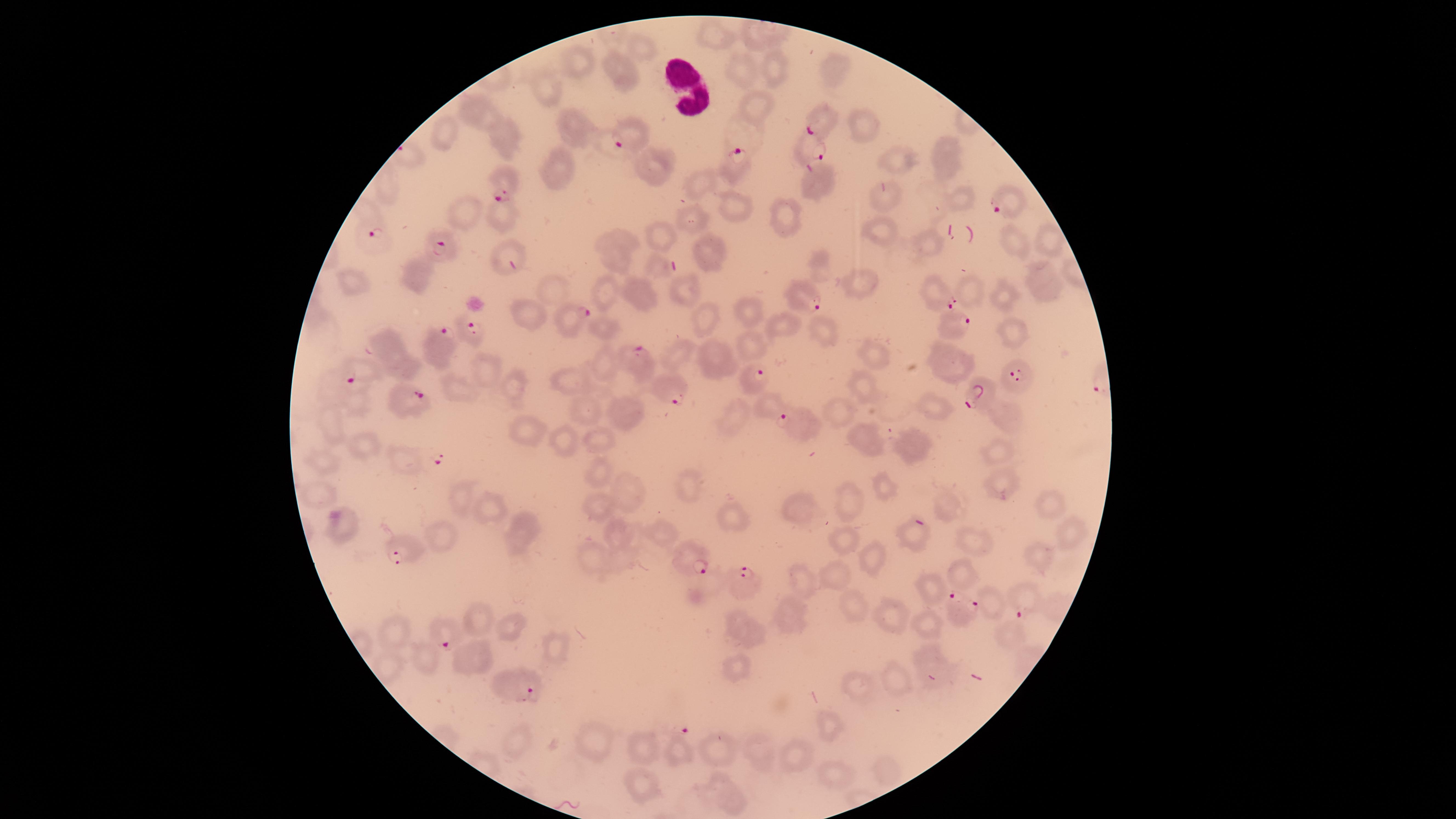
Approximate marker points as [x, y] in pixels. Parasitized red blood cells: [821, 122], [633, 136], [806, 147], [735, 164], [503, 180], [1007, 203], [378, 241], [443, 244], [937, 295], [807, 298], [567, 321], [953, 323], [472, 325], [437, 349], [637, 357], [340, 373], [1020, 378], [752, 379], [664, 387], [977, 395], [410, 398], [797, 424], [399, 540], [685, 561], [746, 581], [1024, 598], [956, 610], [436, 628], [521, 691]. Uninfected red blood cells: [719, 35], [753, 39], [642, 47], [576, 65], [772, 67], [742, 71], [833, 71], [618, 73], [544, 87], [757, 106], [473, 113], [861, 122], [580, 128], [444, 136], [507, 139], [949, 144], [893, 160], [560, 164], [657, 166], [949, 167], [701, 181], [818, 182], [961, 197], [887, 199], [737, 204], [464, 214], [499, 214], [691, 221], [789, 221], [879, 229], [665, 237], [1013, 241], [1048, 241], [928, 245], [613, 247], [715, 249], [502, 251], [422, 275], [1044, 279], [683, 286], [863, 287], [350, 289], [556, 290], [608, 292], [973, 294], [643, 295], [1001, 295], [743, 310], [705, 312], [526, 315], [784, 325], [822, 332], [1020, 334], [387, 345], [759, 348], [875, 352], [682, 355], [715, 361], [947, 361], [606, 364], [405, 367], [484, 369], [511, 383], [573, 383], [865, 384], [457, 388], [356, 400], [771, 406], [938, 408], [842, 411], [591, 413], [1004, 413], [628, 414], [736, 414], [333, 425], [529, 434], [565, 437], [869, 437], [604, 441], [912, 442], [363, 443], [996, 456], [328, 461], [597, 471], [685, 482], [1001, 484], [886, 486], [317, 491], [629, 494], [463, 499], [852, 500], [944, 505], [1043, 505], [605, 507], [801, 509], [497, 510], [734, 512], [521, 529], [1069, 530], [660, 533], [621, 534], [912, 535], [437, 537], [844, 537], [974, 539], [866, 554], [589, 555], [623, 555], [1042, 560], [841, 571], [958, 572], [802, 581], [929, 588], [993, 602], [853, 605], [892, 614], [786, 615], [481, 618], [509, 623], [929, 625], [397, 631], [1013, 634], [750, 635], [554, 645], [426, 652], [476, 660], [931, 662], [735, 672], [897, 679], [860, 688], [824, 724], [515, 741], [592, 741], [645, 745], [678, 748], [760, 751], [723, 754], [795, 756], [885, 770], [832, 775], [642, 782], [724, 793]. Circular visible region. Image is 1456×819 pixels. Photographed with a smartphone camera through the microscope eyepiece. Species: Plasmodium falciparum. Presence: malaria parasites detected. Thin smear of blood. Giemsa-stained preparation. Single field of view.